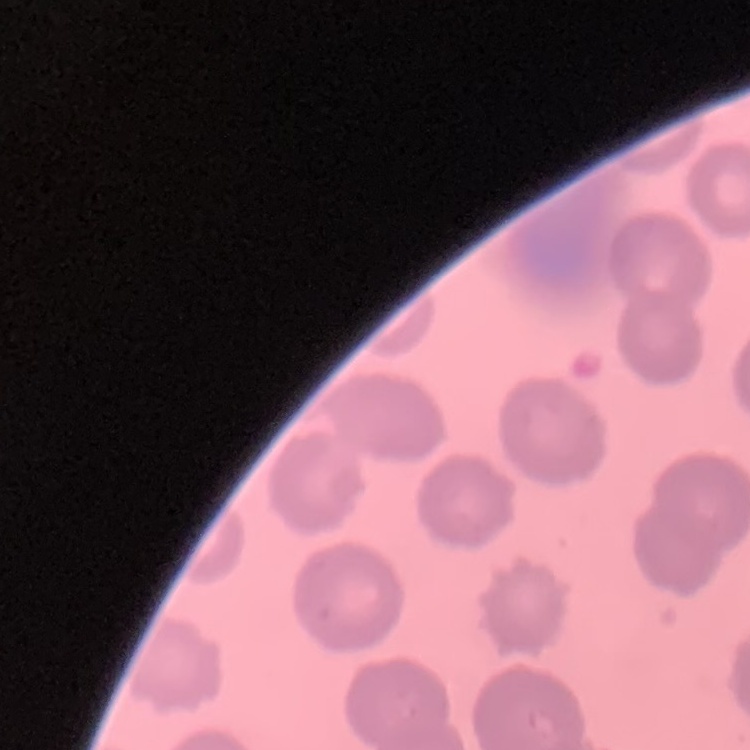
The red blood cells exhibit no rouleaux formation. Field's or Giemsa stain. Thin peripheral smear. One tile cut from a larger photomicrograph.